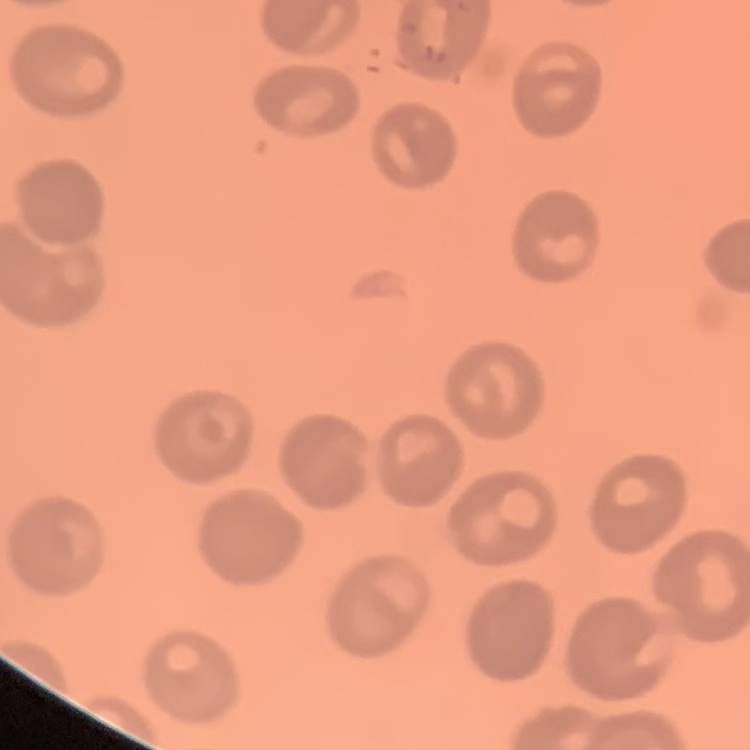
red_blood_cell_morphology: no rouleaux formation
preparation: thin blood film
image_type: square crop of a larger photomicrograph
stain: Field's or Giemsa